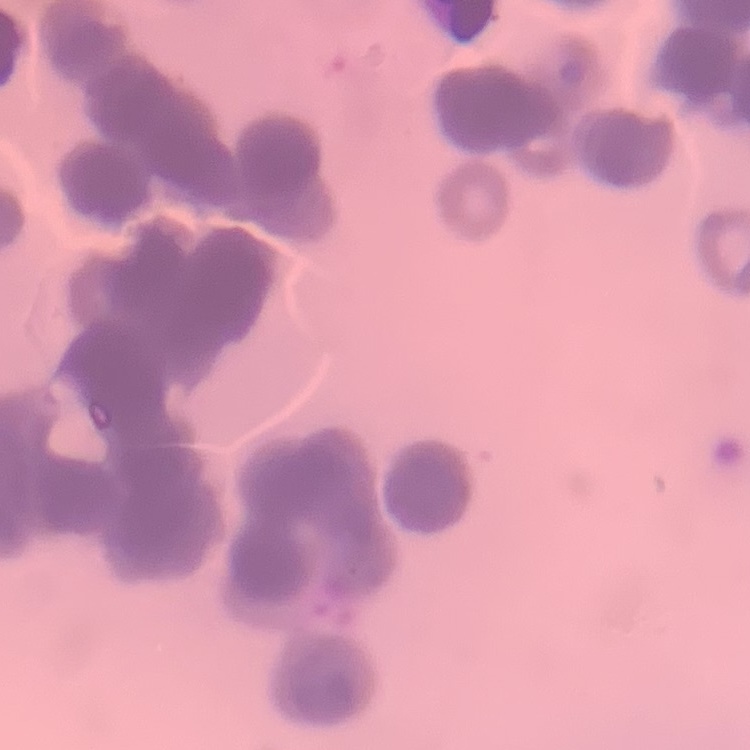
The red blood cells show rouleaux formation. Field's or Giemsa stain. Thin peripheral smear. One tile cut from a larger photomicrograph.